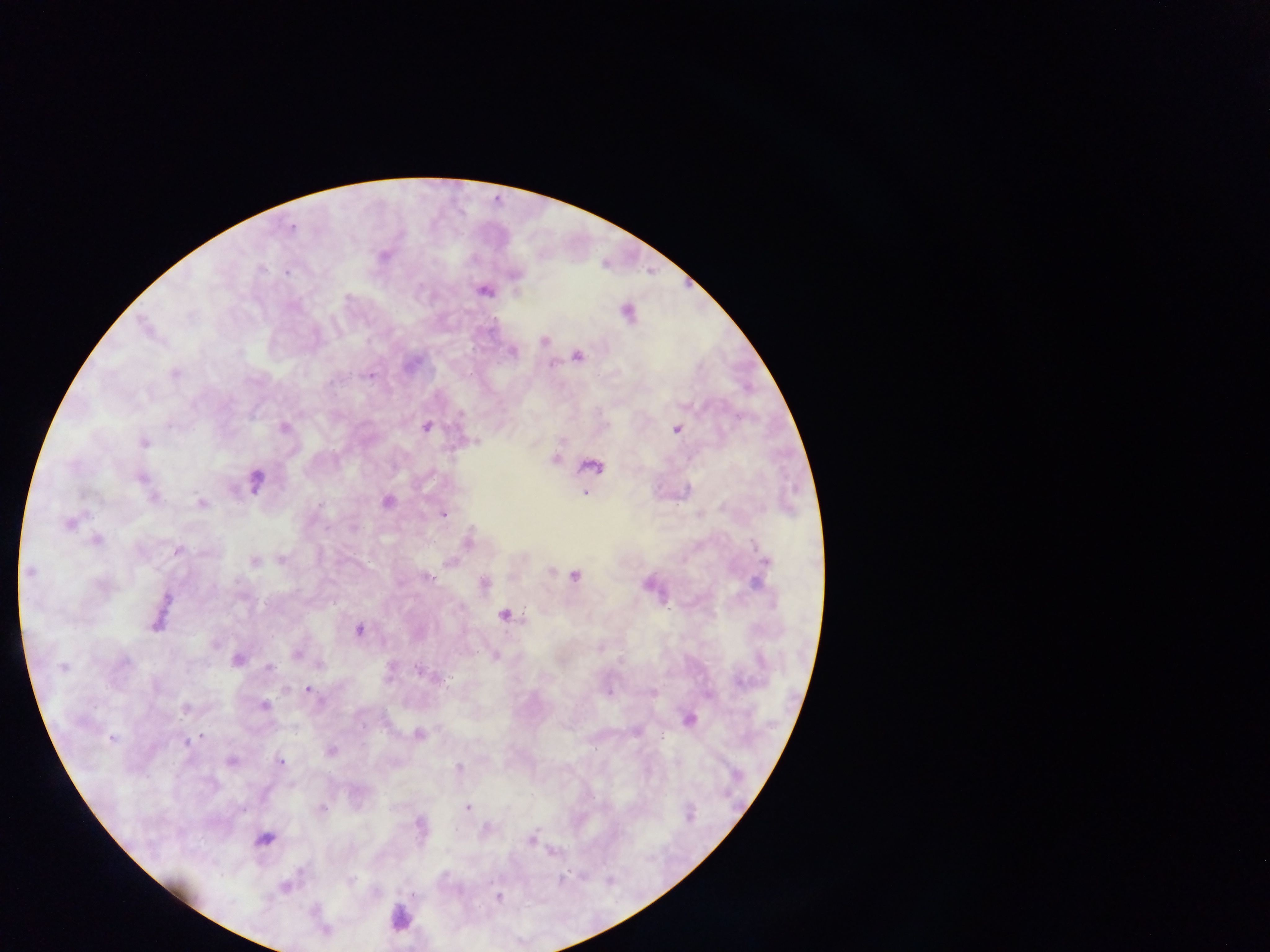
Approximate centers as {x, y} in pixels. Leukocyte locations: {400, 918}. Plasmodium parasite locations: {291, 229}, {383, 256}, {262, 269}, {287, 273}, {514, 275}, {483, 291}, {627, 313}, {544, 341}, {513, 352}, {577, 356}, {174, 373}, {370, 376}, {460, 414}, {426, 427}, {284, 428}, {676, 430}, {144, 443}, {554, 459}, {592, 466}, {142, 478}, {256, 480}, {584, 493}, {153, 497}, {201, 502}, {387, 502}, {319, 505}, {443, 515}, {68, 524}, {97, 539}, {468, 541}, {177, 550}, {282, 560}, {765, 560}, {255, 561}, {450, 562}, {29, 571}, {550, 571}, {575, 576}, {427, 578}, {483, 582}, {757, 583}, {167, 598}, {504, 615}, {155, 625}, {360, 630}, {297, 654}, {495, 657}, {238, 659}, {124, 663}, {63, 668}, {270, 668}, {421, 672}, {308, 690}, {608, 691}, {654, 694}, {264, 706}, {185, 707}, {689, 719}, {363, 726}, {636, 731}, {418, 734}, {202, 736}, {111, 738}, {186, 742}, {331, 751}, {231, 761}, {280, 762}, {458, 767}, {321, 808}, {468, 808}, {242, 809}, {419, 824}, {488, 828}, {264, 839}, {530, 840}, {350, 881}, {285, 887}, {413, 896}, {497, 898}. Mobile-phone photograph taken through the microscope. Thick blood film. Image is 1270×952 pixels. Collected in Ghana. Single field of view.